Classify this cell by malaria status.
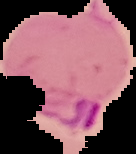
It is parasitized.

Summary:
  - Image size: 136×154 pixels
  - Image type: segmented cell region on a black background
  - Preparation: thin blood film